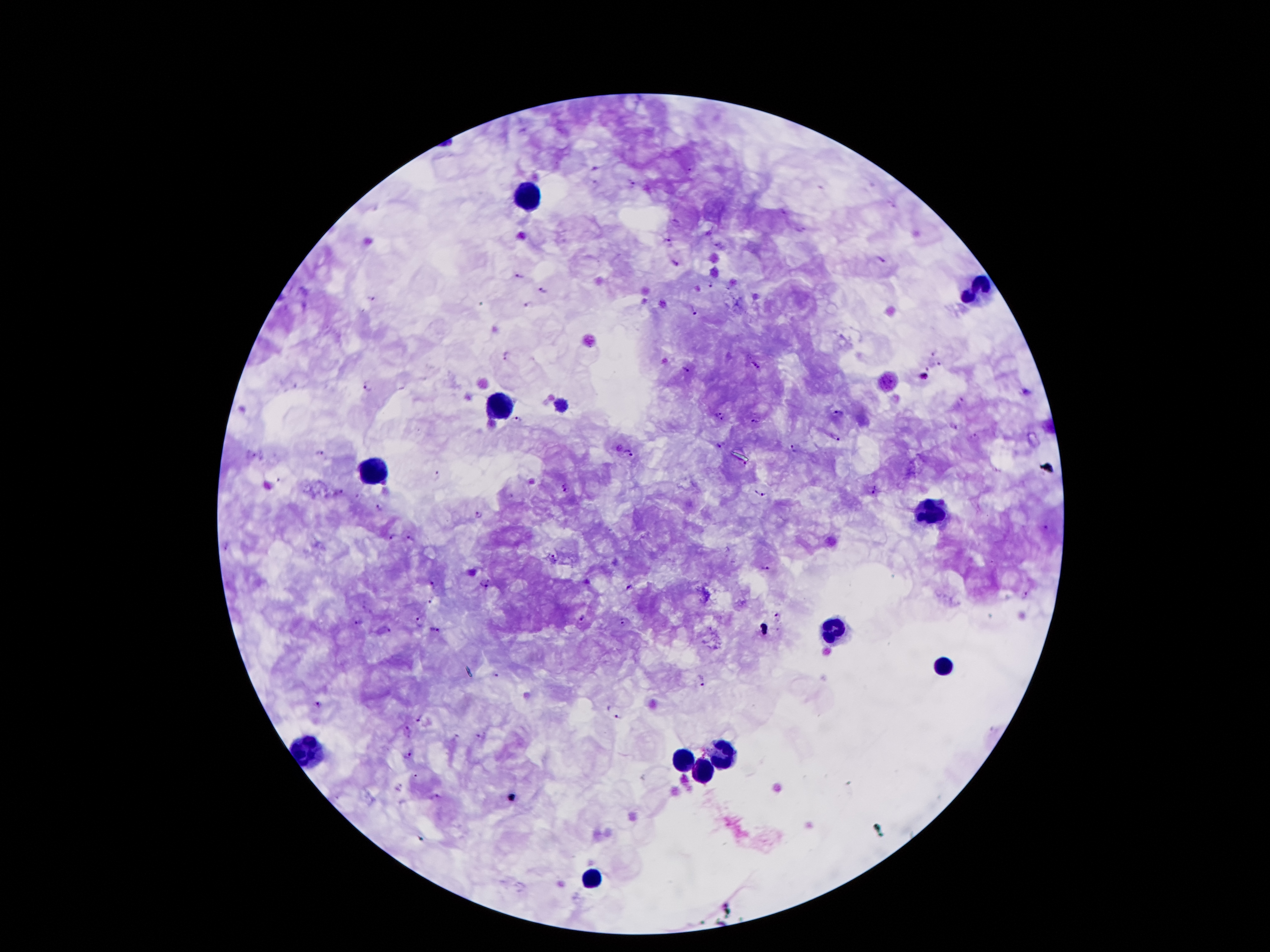 Approximate centers as (x, y) in pixels. Leukocyte locations: (526, 194), (980, 293), (498, 404), (372, 470), (936, 510), (832, 632), (942, 667), (723, 749), (681, 758), (701, 773), (588, 879). Malaria parasite locations: (688, 170), (633, 184), (893, 207), (677, 220), (669, 240), (717, 244), (881, 258), (675, 262), (520, 275), (710, 284), (542, 291), (371, 298), (528, 303), (696, 310), (932, 352), (507, 354), (756, 364), (940, 366), (686, 370), (925, 376), (368, 385), (1026, 393), (961, 400), (717, 412), (838, 412), (517, 418), (722, 420), (755, 421), (954, 425), (838, 437), (977, 437), (717, 446), (793, 446), (620, 447), (322, 453), (631, 453), (745, 464), (437, 477), (566, 487), (875, 490), (341, 491), (761, 494), (380, 507), (480, 515), (391, 538), (410, 539), (552, 556), (765, 569), (485, 582), (433, 584), (630, 587), (428, 601), (778, 614), (582, 619), (419, 620), (625, 621), (359, 622), (388, 628), (434, 629), (496, 673), (703, 680), (319, 705), (619, 715), (419, 718), (408, 730), (482, 737), (408, 755), (399, 787), (511, 797), (438, 798). 100x magnification. Patient malaria status: infected with Plasmodium falciparum. Thick blood smear. Smartphone photograph taken through the microscope eyepiece. Giemsa-stained preparation. Image is 1270×952 pixels. One field from this slide.